Give the preparation type.
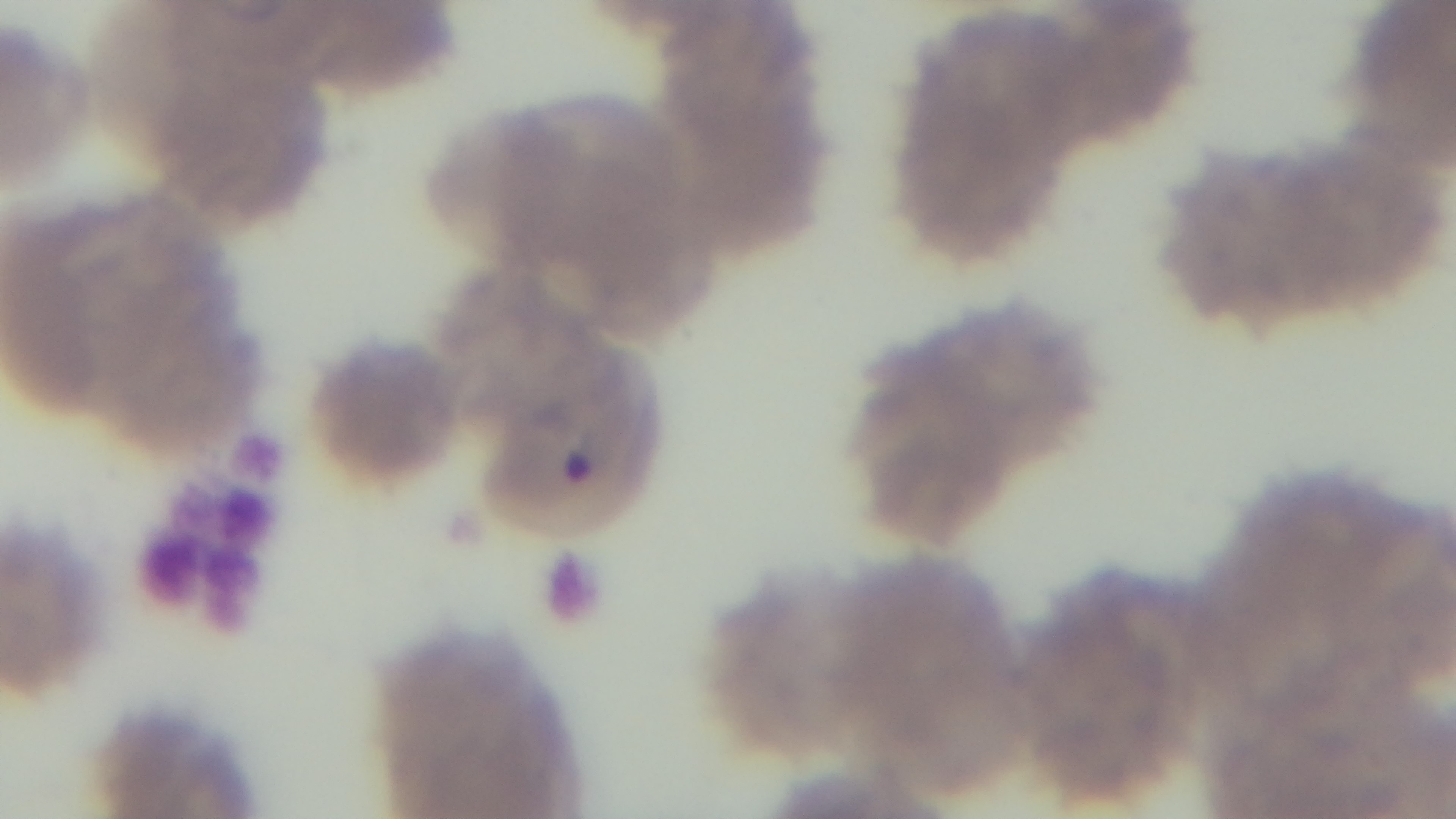
A thin smear.

Summary:
  - Modality: light microscopy
  - Stain: Giemsa
  - Capture: mounted 4K digital camera
  - Field of view: single
  - Objective: 100x oil immersion
  - Malaria status: positive